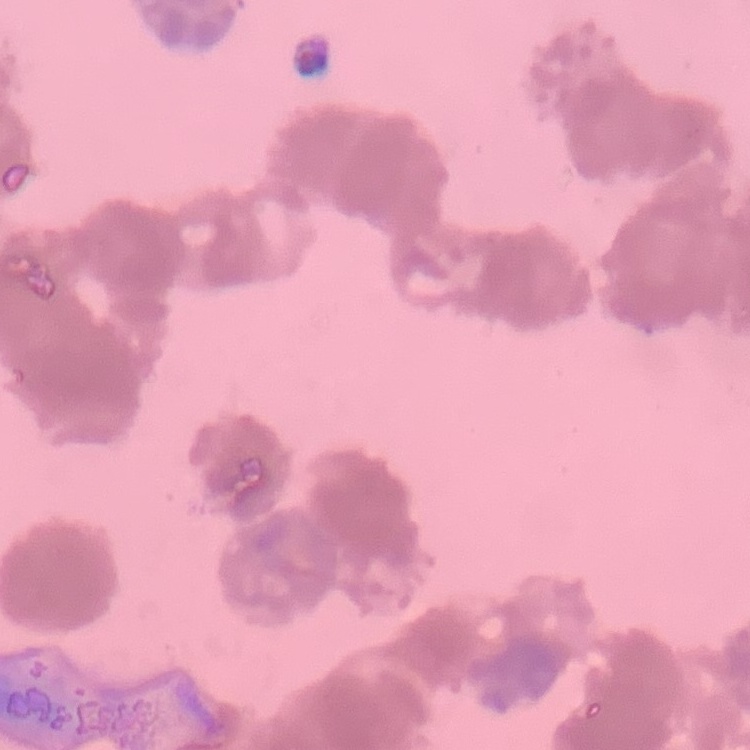
{
  "erythrocyte_morphology": "rouleaux formation",
  "preparation": "thin blood film",
  "image_type": "square crop of a larger photomicrograph",
  "stain": "Field's or Giemsa"
}